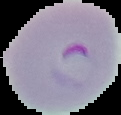 Malaria status: parasitized. From a thin blood smear. Image is 121×115 pixels. The area outside the segmented cell region is set to black.